Classify this cell by malaria status.
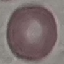
It is uninfected.

Giemsa-stained preparation. Cell patch, automatically extracted from a larger field of view and resized to 64 × 64 pixels. Acquired by smartphone through the microscope eyepiece. Thin blood smear.